Assess for malaria.
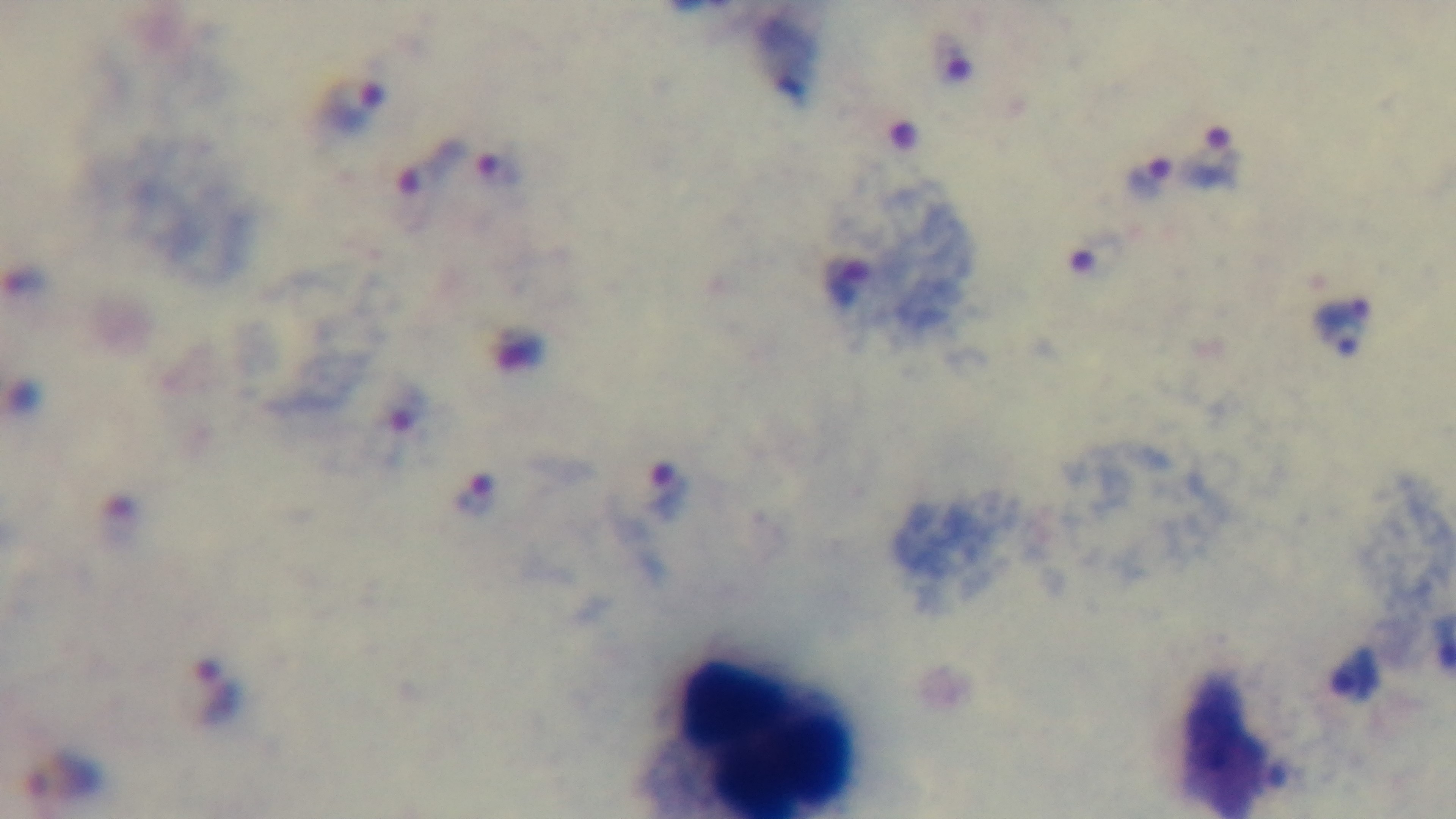
Positive.

capture = mounted 4K digital camera
objective = 100x oil immersion
field of view = one from the slide
modality = light microscopy
stain = Giemsa
preparation = thick